Report the malaria status of this cell.
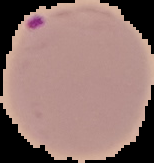

Parasitized.

Summary:
  - Image type: segmented cell region with the area outside set to black
  - Image size: 154×163 pixels
  - Preparation: thin blood film